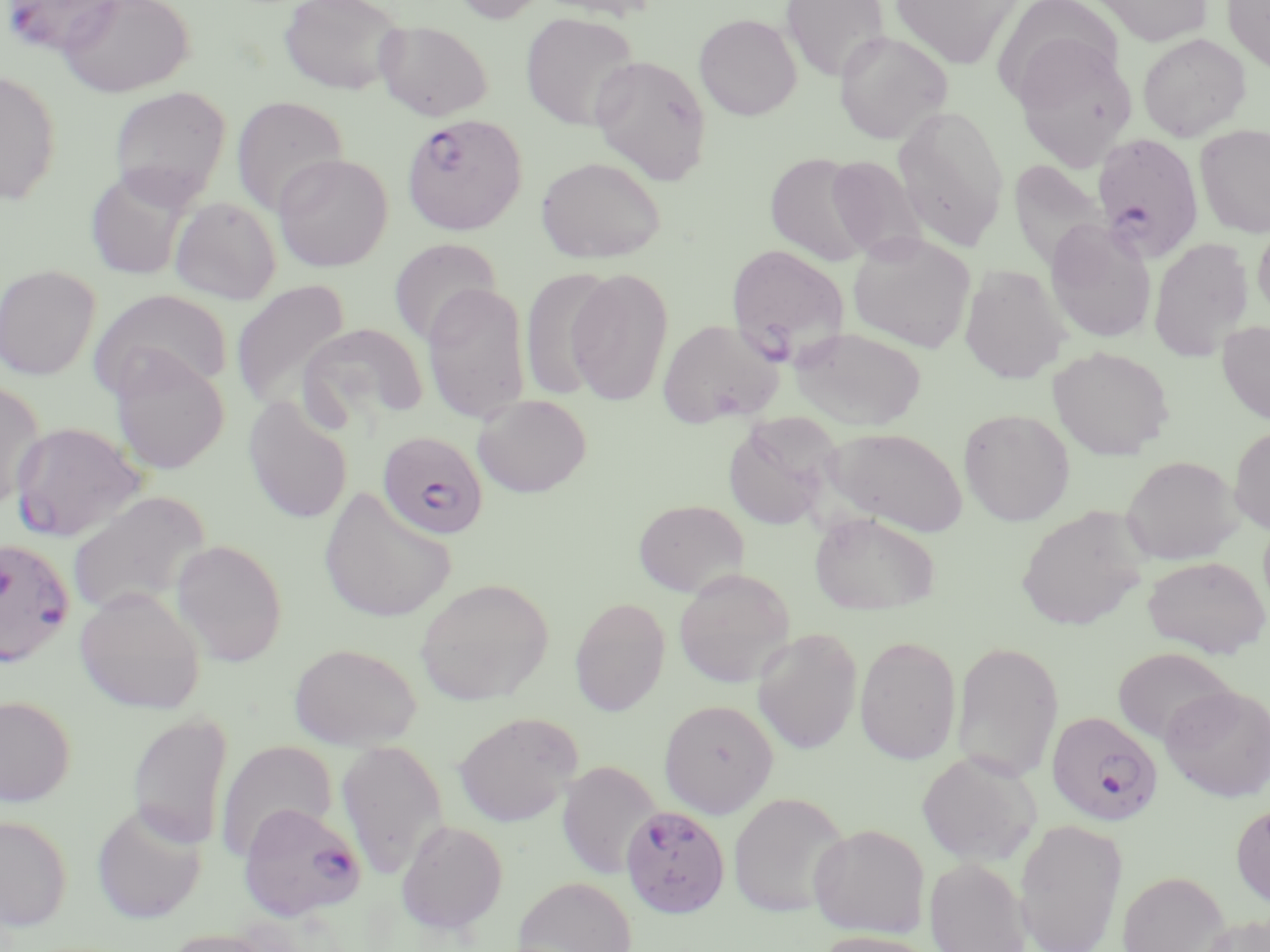

slide_level_diagnosis: Plasmodium falciparum
stain: May-Grünwald-Giemsa
uninfected_red_blood_cell_locations: 'approximate bounding boxes as (x1,y1)-(x2,y2) corner pairs in pixels: (58,0)-(194,97), (279,0)-(407,94), (450,0)-(549,23), (530,0)-(665,21), (780,0)-(891,81), (888,0)-(1023,69), (993,0)-(1124,108), (1089,0)-(1214,47), (1223,0)-(1270,73), (521,12)-(641,131), (694,13)-(801,121), (375,20)-(493,120), (834,30)-(953,144), (1137,33)-(1251,142), (1012,41)-(1138,170), (589,54)-(713,184), (0,70)-(62,205), (108,86)-(231,206), (231,95)-(348,217), (892,105)-(1011,252), (1195,124)-(1270,238), (764,152)-(875,266), (273,153)-(393,272), (823,155)-(928,263), (536,156)-(666,263), (1007,159)-(1111,274), (85,166)-(195,281), (170,196)-(281,304), (1044,219)-(1157,343), (1253,221)-(1270,321), (846,231)-(977,353), (1148,237)-(1254,362), (389,238)-(502,347), (0,264)-(101,381), (959,264)-(1070,384), (521,267)-(617,401), (566,267)-(675,407), (231,279)-(352,411), (422,281)-(531,425), (90,289)-(232,400), (658,318)-(783,428), (1216,319)-(1270,426), (299,323)-(429,429), (790,325)-(927,431), (1048,345)-(1174,460), (109,350)-(230,475), (0,380)-(47,511), (473,394)-(592,497), (243,397)-(352,524), (958,407)-(1075,525), (721,414)-(841,532), (1229,425)-(1270,533), (822,426)-(969,536), (1121,455)-(1242,564), (318,487)-(457,624), (66,490)-(211,618), (633,499)-(749,597), (1016,505)-(1150,631), (809,510)-(941,616), (171,539)-(288,666), (1143,556)-(1269,658), (673,568)-(795,688), (415,578)-(554,705), (74,587)-(206,714), (570,596)-(670,716), (752,627)-(863,754), (855,635)-(961,765), (951,639)-(1065,782), (288,641)-(422,750), (1112,646)-(1236,745), (1160,683)-(1270,802), (0,694)-(76,806), (659,699)-(778,816), (126,710)-(233,852), (453,711)-(582,827), (214,739)-(337,859), (336,739)-(449,879), (917,751)-(1041,867), (556,761)-(661,879), (728,791)-(850,918), (91,802)-(207,924), (1231,802)-(1270,910), (0,815)-(72,931), (396,819)-(508,935), (1013,819)-(1128,952), (808,823)-(930,938), (924,856)-(1031,952), (1117,870)-(1229,952), (512,876)-(637,952), (1192,914)-(1270,952), (159,928)-(281,952), (811,930)-(940,952)'
image_size: 1270×952 pixels
modality: light microscopy
plasmodium_falciparum_infected_red_blood_cell_locations: 'approximate bounding boxes as (x1,y1)-(x2,y2) corner pairs in pixels: (1,0)-(125,56), (401,114)-(528,236), (1091,132)-(1205,264), (726,244)-(852,364), (10,421)-(147,542), (377,430)-(489,540), (0,544)-(76,673), (1046,710)-(1163,827), (238,801)-(366,922), (620,804)-(731,918)'
preparation: thin blood film
field_of_view: one of a larger specimen
magnification: 1000x